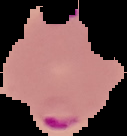
{
  "malaria_status": "parasitized",
  "preparation": "thin blood smear",
  "image_size": "127×136 pixels",
  "image_type": "segmented cell region on a black background"
}